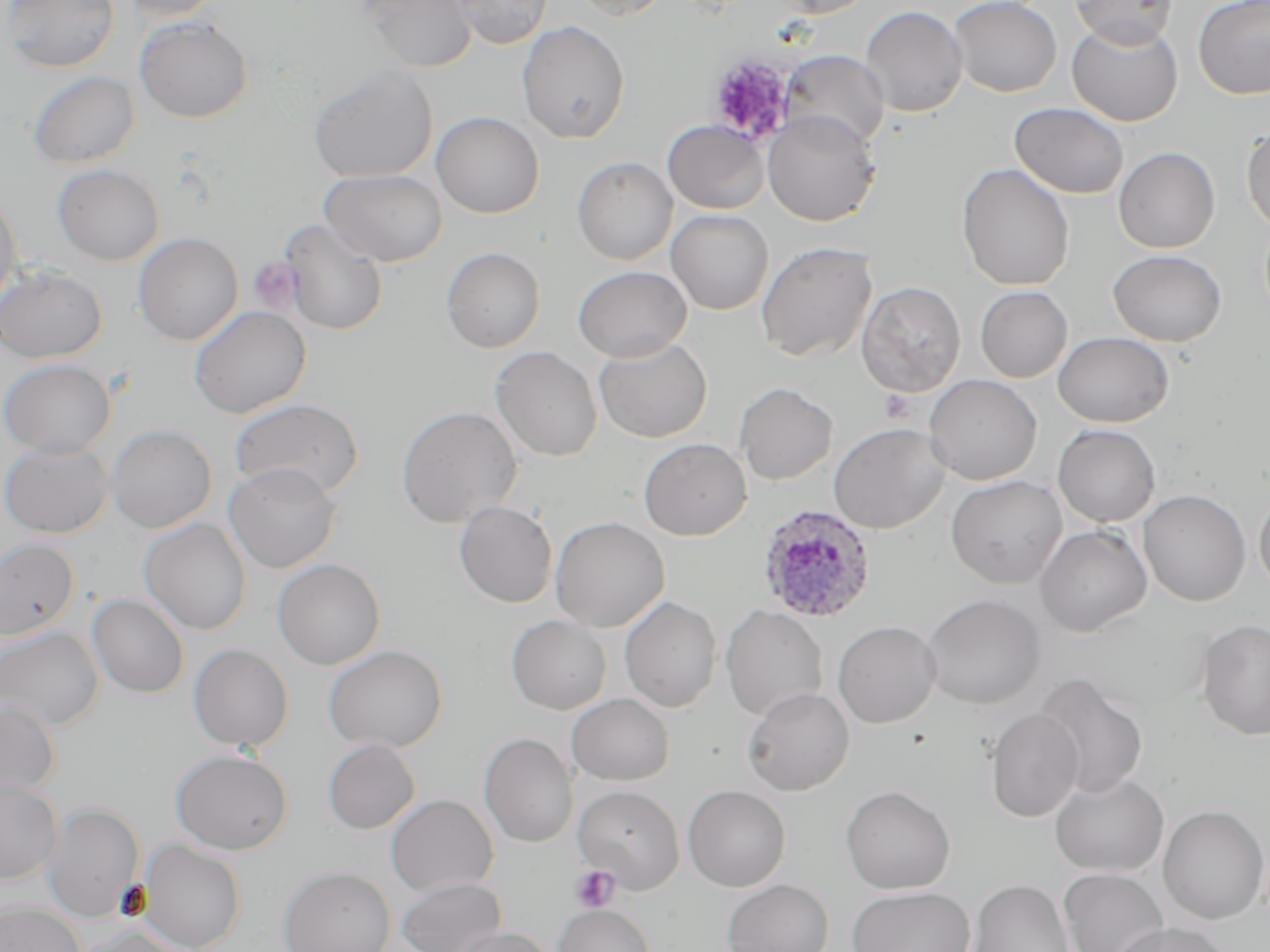
Approximate bounding boxes as (x1,y1)-(x2,y2) corner pairs in pixels. Plasmodium ovale-infected red blood cell locations: (756,503)-(878,624). Platelet locations: (708,54)-(795,145), (248,256)-(304,314), (879,390)-(915,423), (569,864)-(621,913). Uninfected red blood cell locations: (2,0)-(120,73), (118,0)-(229,22), (361,0)-(478,73), (452,0)-(552,49), (567,0)-(674,20), (773,0)-(877,19), (949,0)-(1062,97), (1069,0)-(1179,47), (1193,0)-(1270,99), (860,5)-(968,118), (134,16)-(253,123), (1066,20)-(1184,127), (517,21)-(630,144), (780,50)-(890,150), (308,65)-(438,184), (27,72)-(139,169), (38,73)-(153,261), (1010,102)-(1129,199), (431,111)-(544,219), (762,111)-(880,227), (662,119)-(770,214), (1241,121)-(1270,234), (1113,147)-(1220,253), (572,157)-(678,265), (956,163)-(1075,291), (53,164)-(165,266), (319,169)-(448,267), (0,192)-(23,312), (665,209)-(773,315), (279,219)-(389,337), (133,232)-(243,345), (756,241)-(877,363), (441,246)-(546,353), (1108,249)-(1226,347), (573,265)-(693,362), (0,266)-(108,364), (855,281)-(966,397), (974,285)-(1072,383), (189,305)-(311,419), (1052,331)-(1175,427), (593,336)-(713,443), (490,347)-(603,462), (0,358)-(116,458), (924,374)-(1042,485), (734,382)-(838,485), (228,398)-(365,500), (396,405)-(523,528), (828,422)-(951,534), (1052,424)-(1160,527), (106,425)-(217,534), (637,438)-(752,541), (0,439)-(113,539), (223,462)-(343,574), (946,475)-(1067,589), (1138,489)-(1251,606), (1254,491)-(1270,596), (454,500)-(558,608), (550,516)-(670,632), (139,517)-(252,635), (1035,524)-(1152,637), (0,538)-(80,641), (272,558)-(386,670), (87,595)-(189,698), (921,595)-(1044,709), (619,596)-(722,713), (720,605)-(828,721), (506,614)-(611,715), (1198,619)-(1270,740), (833,620)-(940,728), (0,626)-(104,730), (188,644)-(294,751), (323,645)-(448,753), (1034,672)-(1149,799), (742,687)-(854,796), (567,693)-(675,786), (0,699)-(61,799), (984,708)-(1084,823), (479,732)-(579,848), (322,738)-(420,834), (170,748)-(293,855), (1049,772)-(1169,877), (0,779)-(63,883), (573,784)-(685,893), (841,784)-(956,894), (683,785)-(791,892), (386,794)-(499,897), (41,803)-(145,921), (1157,805)-(1269,924), (137,839)-(247,952), (279,866)-(395,952), (1058,867)-(1169,952), (397,876)-(507,952), (722,879)-(833,952), (968,879)-(1075,952), (846,886)-(976,952), (0,902)-(84,952), (554,904)-(655,952), (1110,922)-(1233,952), (69,926)-(191,952), (450,927)-(559,952). Slide-level diagnosis: Plasmodium ovale. May-Grünwald-Giemsa stain. Image is 1270×952 pixels. Light microscopy. One field of a larger specimen. 1000x magnification. Thin blood smear.